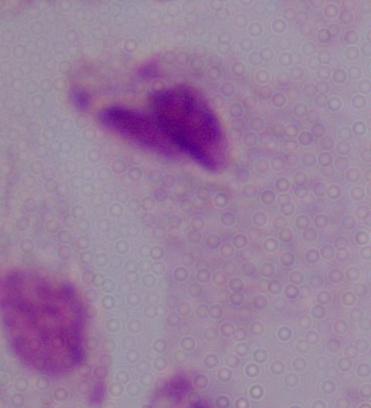

identification = trichomonad
magnification = 1000x
modality = micrograph